State which parasite is depicted.
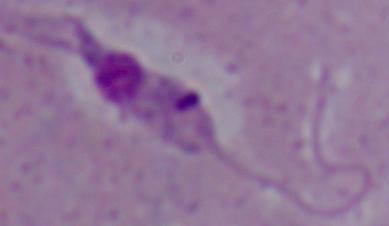
Leishmania.

Micrograph. Captured at 1000x magnification.